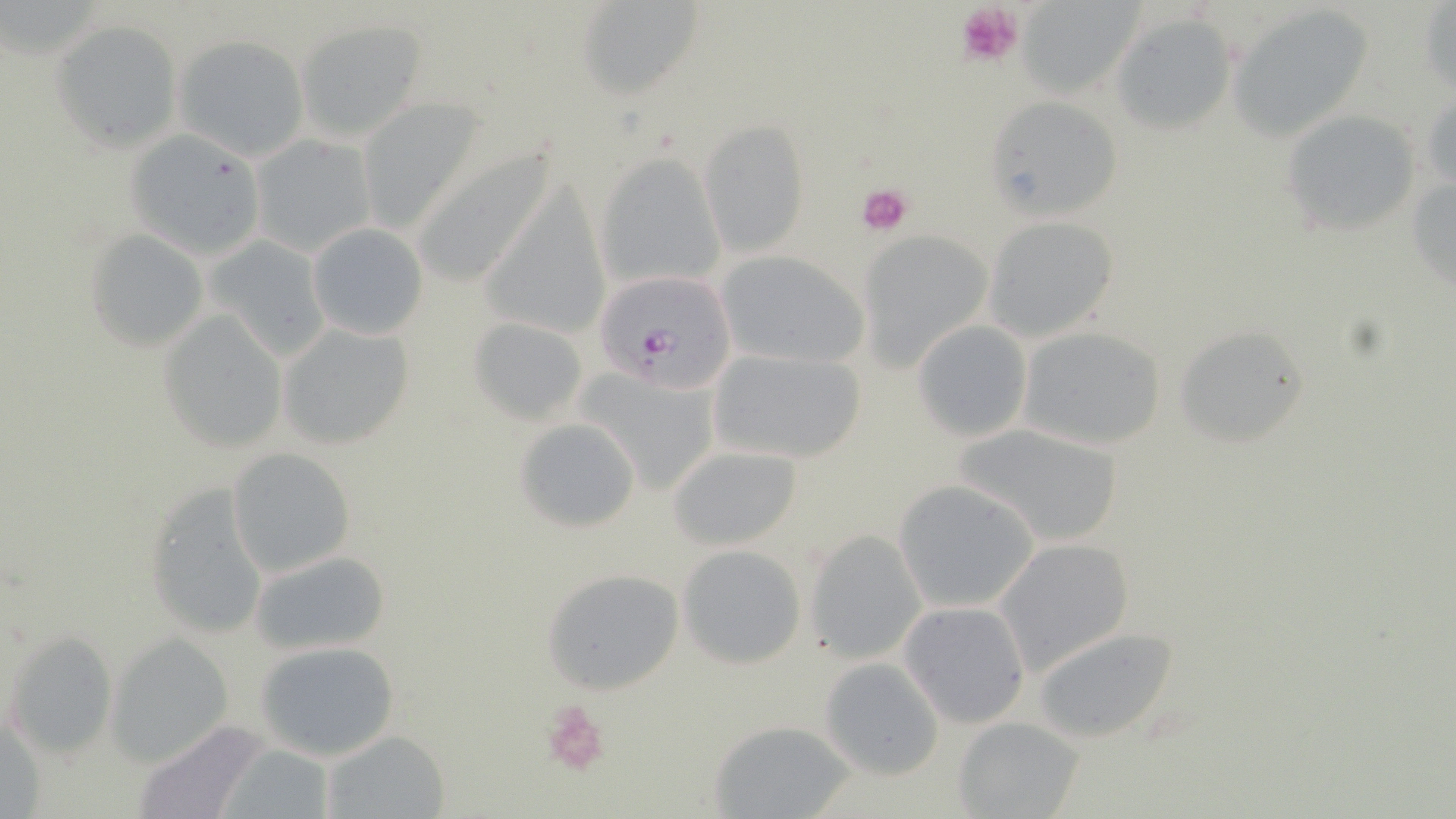
slide-level diagnosis = Plasmodium falciparum
uninfected red blood cell locations = approximate bounding boxes as (x1,y1)-(x2,y2) corner pairs in pixels: (579,1)-(700,98), (1016,2)-(1142,97), (1421,3)-(1455,94), (1228,5)-(1374,138), (1112,12)-(1239,135), (296,19)-(428,140), (53,20)-(182,148), (175,35)-(308,159), (991,95)-(1136,228), (1282,110)-(1423,232), (702,119)-(809,255), (125,131)-(268,260), (252,134)-(377,258), (409,142)-(560,291), (596,154)-(726,292), (1407,168)-(1455,298), (981,216)-(1117,341), (306,223)-(429,340), (84,231)-(207,350), (861,232)-(995,366), (206,234)-(334,358), (716,250)-(869,369), (159,311)-(286,450), (470,317)-(590,424), (913,321)-(1033,443), (275,322)-(416,452), (1172,323)-(1314,448), (1016,325)-(1169,450), (705,346)-(870,465), (572,366)-(723,497), (514,416)-(641,534), (952,422)-(1129,547), (665,444)-(805,552), (227,448)-(355,577), (142,478)-(272,641), (895,479)-(1041,613), (803,530)-(926,663), (992,537)-(1135,676), (677,544)-(807,668), (248,547)-(389,655), (542,568)-(683,693), (899,601)-(1031,728), (1030,626)-(1180,744), (5,630)-(118,759), (105,631)-(234,766), (254,640)-(401,762), (820,656)-(946,780), (954,716)-(1087,819), (131,721)-(272,819), (707,722)-(855,815), (322,730)-(450,818), (219,741)-(341,819)
field of view = single
Plasmodium falciparum-infected red blood cell locations = approximate bounding boxes as (x1,y1)-(x2,y2) corner pairs in pixels: (593,270)-(739,393)
preparation = thin blood smear
stain = May-Grünwald-Giemsa
image size = 1456×819 pixels
platelet locations = approximate bounding boxes as (x1,y1)-(x2,y2) corner pairs in pixels: (955,1)-(1022,66), (855,181)-(915,237), (541,697)-(612,778)
modality = light microscopy
magnification = 1000x